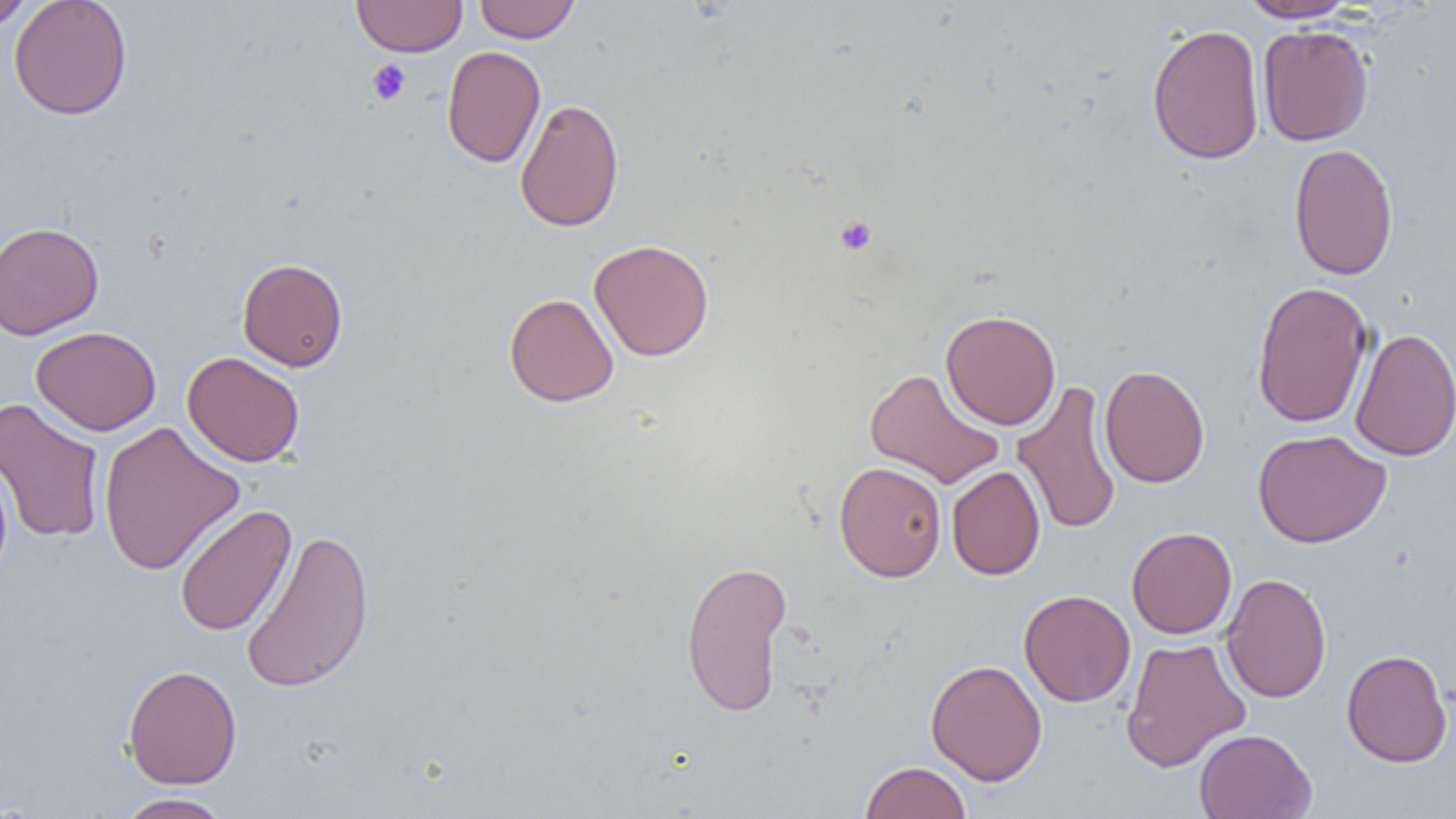
Approximate bounding boxes as named x1/y1/x2/y2 corners in pixels. Uninfected red blood cell locations: (x1=0, y1=0, x2=36, y2=31), (x1=8, y1=0, x2=132, y2=120), (x1=351, y1=0, x2=467, y2=57), (x1=474, y1=0, x2=579, y2=43), (x1=1237, y1=0, x2=1360, y2=23), (x1=1146, y1=23, x2=1265, y2=165), (x1=1257, y1=24, x2=1374, y2=146), (x1=441, y1=45, x2=545, y2=168), (x1=515, y1=98, x2=624, y2=233), (x1=1288, y1=142, x2=1399, y2=281), (x1=0, y1=221, x2=104, y2=340), (x1=589, y1=239, x2=714, y2=362), (x1=237, y1=257, x2=348, y2=371), (x1=1251, y1=281, x2=1374, y2=428), (x1=504, y1=293, x2=619, y2=407), (x1=940, y1=309, x2=1061, y2=430), (x1=31, y1=326, x2=161, y2=435), (x1=1349, y1=327, x2=1456, y2=462), (x1=182, y1=352, x2=305, y2=467), (x1=1099, y1=364, x2=1210, y2=488), (x1=864, y1=368, x2=1005, y2=489), (x1=1011, y1=380, x2=1122, y2=537), (x1=0, y1=396, x2=106, y2=544), (x1=97, y1=420, x2=245, y2=576), (x1=1252, y1=429, x2=1391, y2=548), (x1=0, y1=453, x2=13, y2=582), (x1=834, y1=461, x2=947, y2=581), (x1=946, y1=465, x2=1045, y2=581), (x1=174, y1=504, x2=296, y2=637), (x1=1126, y1=526, x2=1237, y2=639), (x1=242, y1=528, x2=375, y2=694), (x1=681, y1=559, x2=792, y2=717), (x1=1220, y1=572, x2=1332, y2=704), (x1=1019, y1=589, x2=1135, y2=707), (x1=1120, y1=637, x2=1251, y2=772), (x1=1341, y1=649, x2=1452, y2=768), (x1=925, y1=659, x2=1047, y2=785), (x1=123, y1=664, x2=242, y2=789), (x1=1194, y1=728, x2=1318, y2=818), (x1=859, y1=761, x2=972, y2=819), (x1=114, y1=793, x2=233, y2=819). Platelet locations: (x1=366, y1=59, x2=411, y2=106), (x1=834, y1=215, x2=878, y2=256). Slide-level diagnosis: no evidence of blood parasites. Light microscopy. One field of a larger specimen. Image is 1456×819 pixels. 1000x magnification. Thin blood smear.